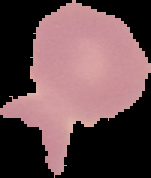

Image is 151×178 pixels. Segmented cell region on a black background. From a thin blood smear. Result: no Plasmodium parasites seen.